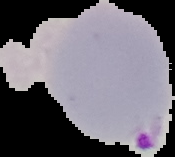

Summary:
  - Image size: 175×157 pixels
  - Preparation: thin blood smear
  - Result: malaria parasites detected
  - Image type: cell region segmented out of the field of view; surrounding area masked to black